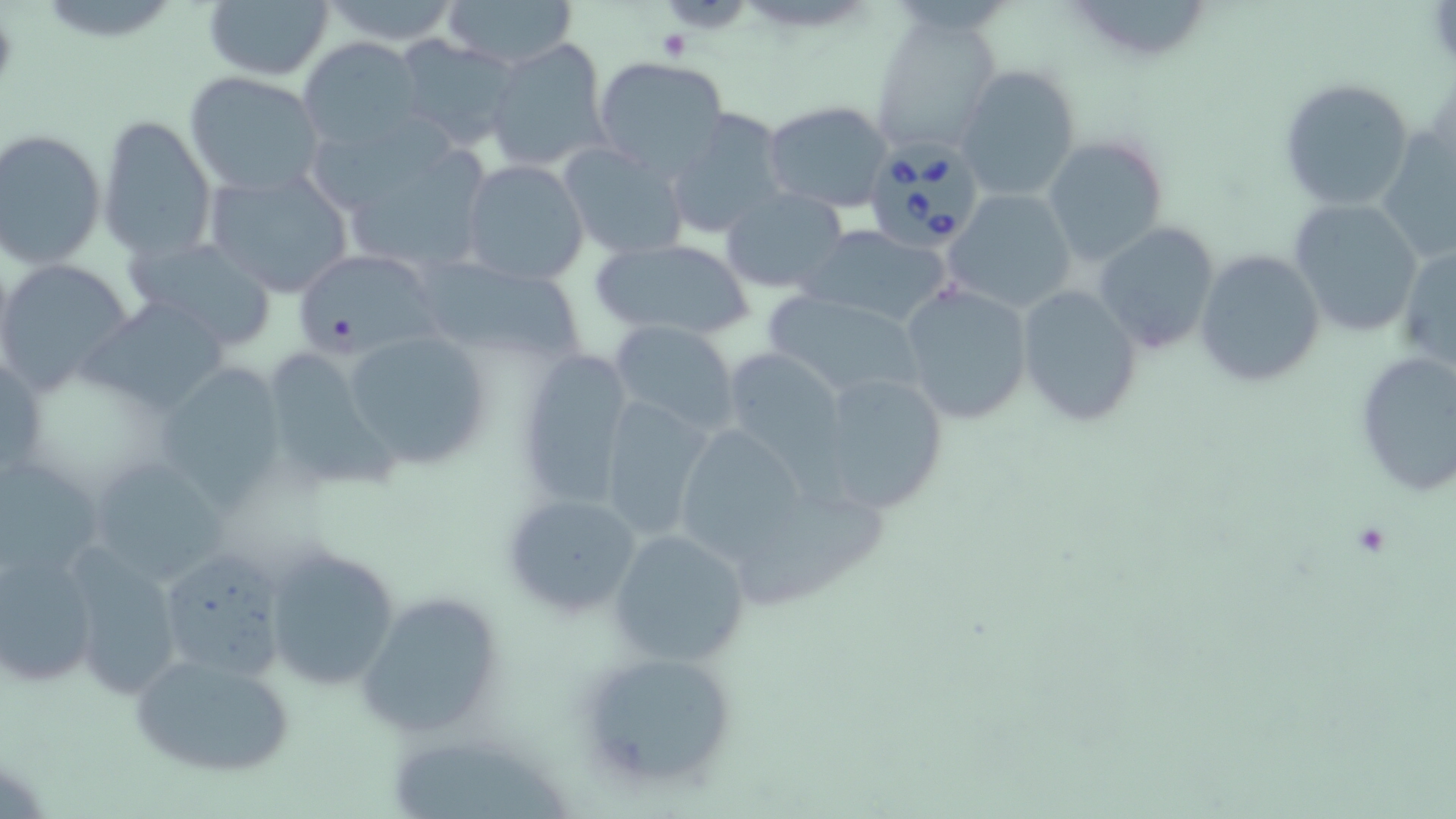

{
  "babesia_divergens_infected_red_blood_cell_locations": "approximate bounding boxes as (x1, y1, x2, y2) in pixels: (870, 148, 976, 249)",
  "slide_level_diagnosis": "Babesia divergens",
  "image_size": "1456×819 pixels",
  "modality": "light microscopy",
  "stain": "May-Grünwald-Giemsa",
  "magnification": "1000x",
  "preparation": "thin blood film",
  "field_of_view": "one of a larger specimen",
  "uninfected_red_blood_cell_locations": "approximate bounding boxes as (x1, y1, x2, y2) in pixels: (441, 0, 578, 68), (1059, 0, 1219, 65), (202, 1, 334, 81), (316, 1, 465, 48), (869, 18, 1002, 158), (299, 37, 424, 149), (392, 37, 521, 151), (484, 37, 612, 173), (592, 56, 731, 177), (954, 63, 1083, 203), (183, 71, 325, 196), (1278, 78, 1419, 214), (762, 101, 895, 213), (663, 107, 791, 241), (97, 113, 217, 260), (1381, 127, 1455, 264), (1, 128, 105, 267), (1042, 134, 1169, 268), (332, 140, 494, 277), (556, 142, 688, 261), (461, 160, 590, 287), (204, 167, 356, 297), (720, 187, 849, 295), (943, 189, 1078, 315), (1287, 198, 1425, 338), (1091, 221, 1219, 354), (795, 222, 956, 331), (128, 237, 279, 351), (590, 238, 757, 342), (1397, 245, 1456, 375), (291, 248, 439, 357), (1195, 250, 1325, 388), (1, 259, 134, 395), (419, 259, 587, 362), (900, 280, 1034, 425), (1016, 284, 1144, 427), (760, 291, 930, 402), (84, 296, 230, 415), (607, 322, 739, 438), (344, 330, 493, 470), (719, 345, 849, 470), (255, 346, 404, 494), (512, 348, 633, 511), (1353, 350, 1455, 496), (0, 354, 47, 483), (148, 363, 289, 507), (814, 370, 951, 514), (597, 394, 718, 543), (682, 429, 801, 561), (0, 453, 107, 583), (84, 454, 233, 591), (724, 486, 883, 613), (501, 491, 644, 621), (609, 527, 751, 668), (263, 543, 403, 691), (156, 545, 290, 680), (1, 548, 100, 689), (65, 550, 184, 701), (355, 594, 502, 738), (127, 647, 297, 780), (573, 648, 740, 791), (392, 745, 563, 816)",
  "platelet_locations": "approximate bounding boxes as (x1, y1, x2, y2) in pixels: (653, 27, 697, 63)"
}